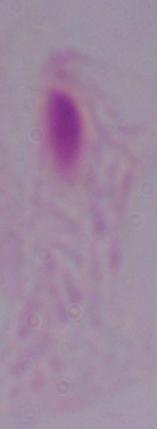

A trichomonad is shown. 1000x magnification. Micrograph.